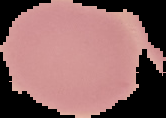
{
  "image_type": "cell region segmented out of the field of view; surrounding area masked to black",
  "image_size": "166×118 pixels",
  "malaria_status": "uninfected",
  "preparation": "thin blood film"
}